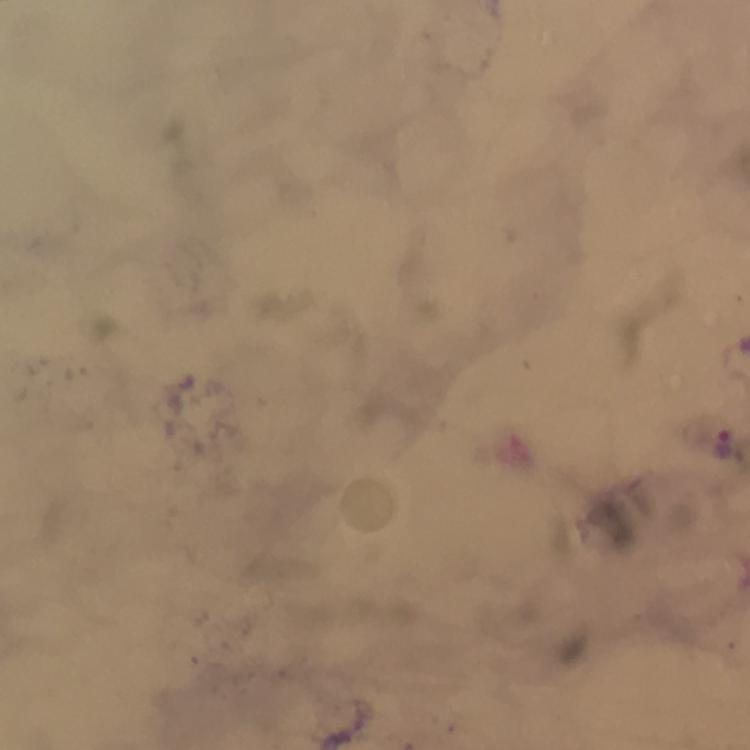
stain = Giemsa
capture = smartphone camera through the microscope
cropped from = a single field of view
context = from a diagnostic examination for malaria
immersion oil = applied
preparation = thick smear
image size = 750×750 pixels
Plasmodium parasite locations = approximate centers as [x, y] in pixels: [722, 444]
magnification = 100x